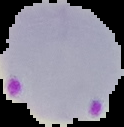

Malaria status: parasitized. From a thin blood smear. Image is 124×127 pixels. The area outside the segmented cell region is set to black.